Identify the blood parasite species.
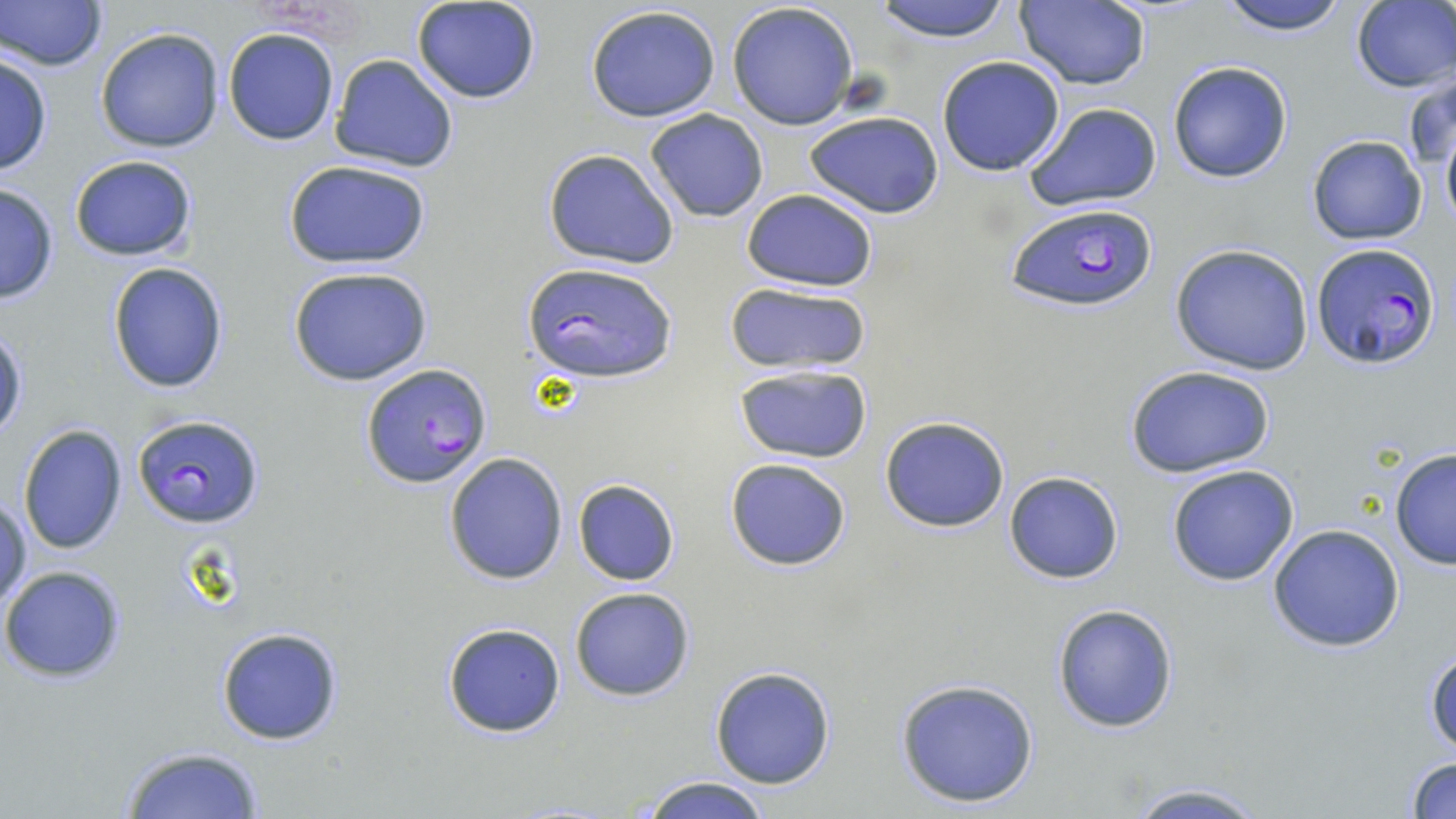

Plasmodium falciparum.

stain = May-Grünwald-Giemsa
uninfected red blood cell locations = approximate bounding boxes as (x1,y1)-(x2,y2) corner pairs in pixels: (1,0)-(106,71), (413,0)-(542,104), (870,0)-(1018,44), (1014,0)-(1153,92), (1215,0)-(1350,38), (1349,1)-(1456,91), (727,3)-(861,130), (585,5)-(722,123), (95,26)-(224,153), (223,27)-(340,146), (222,39)-(456,158), (0,52)-(52,178), (329,54)-(459,173), (936,56)-(1067,176), (1166,60)-(1294,184), (1404,71)-(1455,185), (1022,101)-(1162,211), (644,109)-(768,223), (804,110)-(945,219), (1439,113)-(1456,237), (1306,134)-(1428,245), (542,147)-(680,269), (68,155)-(198,261), (282,159)-(432,270), (0,182)-(60,305), (739,189)-(881,291), (1168,242)-(1318,375), (107,262)-(230,393), (289,267)-(435,387), (722,281)-(873,377), (0,327)-(26,441), (1125,363)-(1279,480), (734,364)-(873,464), (879,416)-(1012,533), (18,423)-(128,555), (1389,446)-(1456,570), (443,452)-(568,584), (725,458)-(851,571), (1165,463)-(1301,587), (1003,470)-(1126,585), (572,478)-(679,585), (0,491)-(30,612), (1266,524)-(1406,651), (1,566)-(125,682), (569,587)-(696,701), (1051,602)-(1180,733), (442,622)-(567,737), (216,626)-(344,746), (1426,645)-(1456,759), (709,666)-(836,789), (892,677)-(1042,809), (117,745)-(264,819), (1404,755)-(1456,818), (637,775)-(775,819), (1117,780)-(1276,819)
field of view = one of a larger specimen
Plasmodium falciparum-infected red blood cell locations = approximate bounding boxes as (x1,y1)-(x2,y2) corner pairs in pixels: (1004,200)-(1162,313), (1311,244)-(1442,367), (524,261)-(676,384), (362,364)-(492,488), (132,414)-(264,529)
modality = light microscopy
preparation = thin blood film
image size = 1456×819 pixels
magnification = 1000x